Locate platelets.
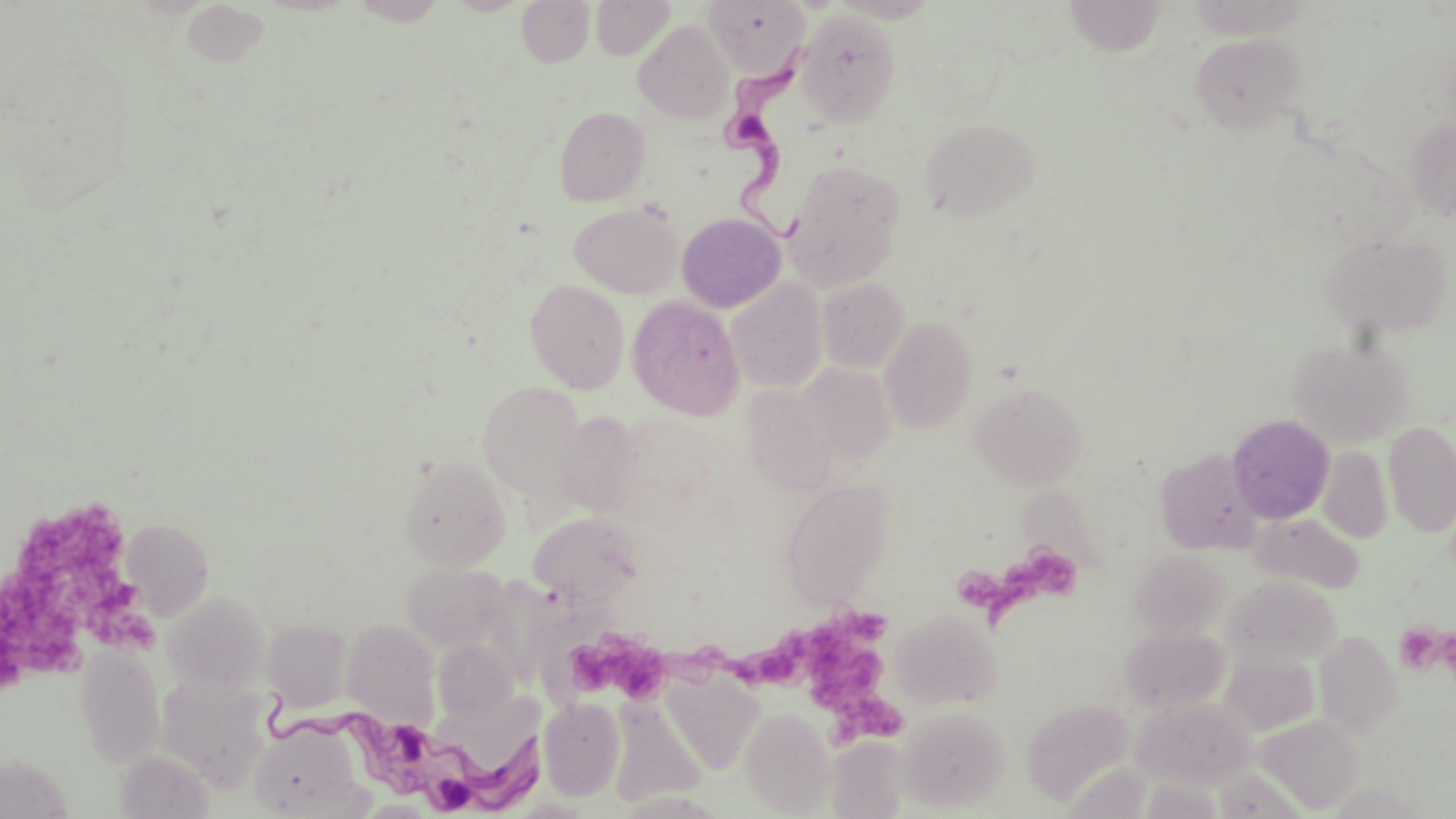

Approximate bounding boxes as (x1,y1)-(x2,y2) corner pairs in pixels.
Platelets: (20,506)-(129,581), (1008,546)-(1079,613), (0,558)-(88,674), (960,566)-(1027,628), (78,574)-(169,654), (845,607)-(893,644), (1394,623)-(1443,673), (567,627)-(708,702), (731,631)-(826,690), (808,637)-(916,746).

Summary:
  - Trypanosoma brucei locations: (715,33)-(814,234), (261,687)-(546,814)
  - Uninfected red blood cell locations: (516,0)-(594,67), (591,0)-(674,60), (1065,0)-(1165,56), (706,1)-(808,75), (796,9)-(901,126), (634,19)-(734,124), (1190,33)-(1304,133), (554,107)-(650,205), (1404,116)-(1456,222), (919,119)-(1040,222), (784,159)-(906,289), (569,200)-(683,298), (676,212)-(786,313), (1321,231)-(1453,336), (817,278)-(909,373), (526,279)-(630,393), (726,279)-(827,393), (627,295)-(745,420), (879,316)-(978,433), (1289,336)-(1413,448), (799,362)-(896,463), (478,381)-(586,497), (970,382)-(1087,489), (741,383)-(836,494), (552,412)-(643,515), (1227,415)-(1335,523), (1384,422)-(1456,537), (1318,445)-(1393,543), (1154,447)-(1262,555), (398,455)-(511,571), (779,478)-(895,607), (1250,511)-(1365,593), (529,512)-(643,606), (121,519)-(214,620), (1130,551)-(1230,639), (402,562)-(510,651), (1224,574)-(1341,665), (162,593)-(269,694), (890,609)-(1001,709), (262,619)-(352,712), (342,619)-(440,724), (1121,627)-(1231,713), (1314,630)-(1402,736), (433,640)-(518,723), (76,643)-(165,768), (1221,651)-(1320,735), (662,670)-(765,775), (157,676)-(272,790), (608,695)-(706,808), (1133,696)-(1256,787), (539,697)-(625,800), (1021,698)-(1134,806), (898,706)-(1009,812), (739,707)-(836,816), (1257,715)-(1363,813), (249,720)-(362,818), (827,736)-(910,818), (115,750)-(215,818), (1,753)-(73,817), (1212,769)-(1302,818)
  - Slide-level diagnosis: Trypanosoma brucei
  - Field of view: single
  - Modality: light microscopy
  - Magnification: 1000x
  - Stain: May-Grünwald-Giemsa
  - Preparation: thin blood smear
  - Image size: 1456×819 pixels